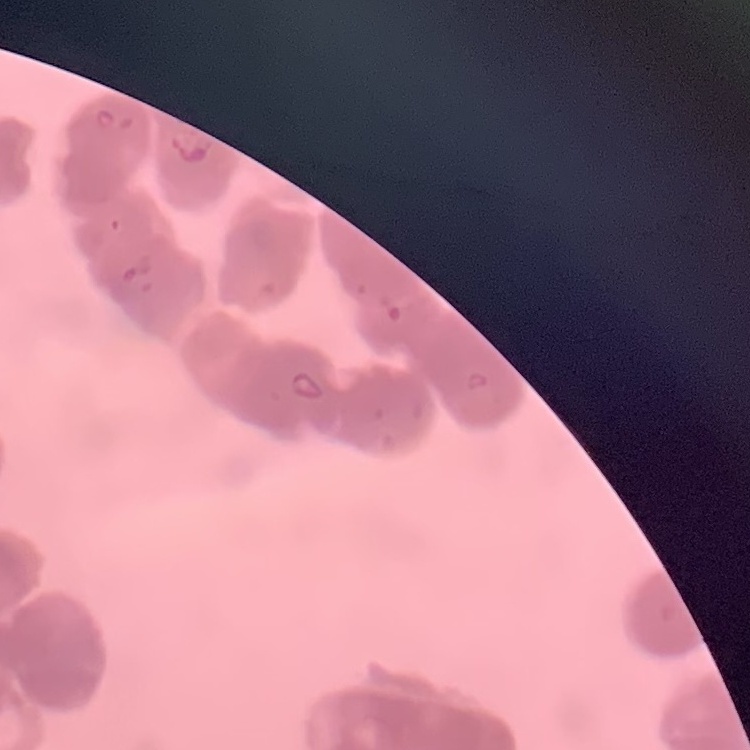
erythrocyte morphology = rouleaux formation
image type = one tile cut from a larger photomicrograph
stain = Field's or Giemsa
preparation = thin peripheral smear